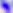
Toxoplasma gondii is shown. Captured at 400x magnification. Micrograph.